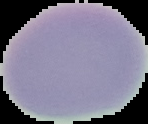
Image is 148×124 pixels. The area outside the segmented cell region is set to black. Malaria status: uninfected. From a thin blood smear.